Identify the cell.
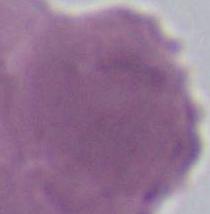
An erythrocyte.

1000x magnification. Micrograph.